Assess this cell for malaria.
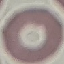
Uninfected.

Thin blood film. Giemsa stain. Acquired by smartphone through the microscope eyepiece. Cell patch, automatically extracted from a larger field of view and resized to 64 × 64 pixels.